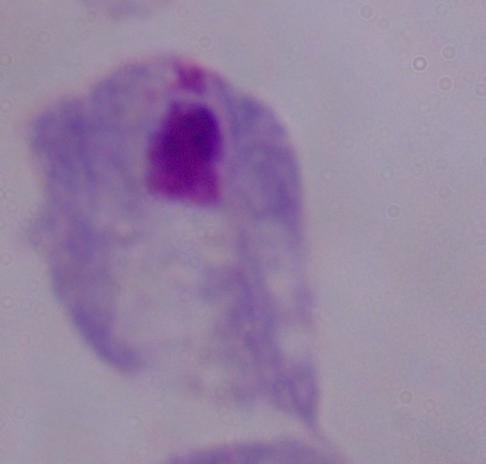

Photomicrograph. Captured at 1000x magnification. A trichomonad is shown.